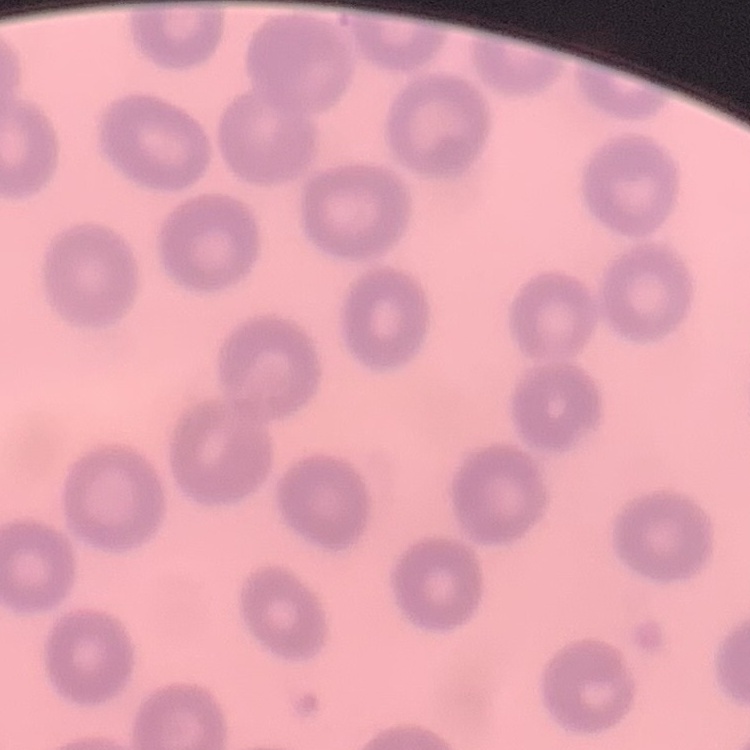

red_blood_cell_morphology: no rouleaux formation
image_type: square crop of a larger photomicrograph
preparation: thin blood smear
stain: Field's or Giemsa